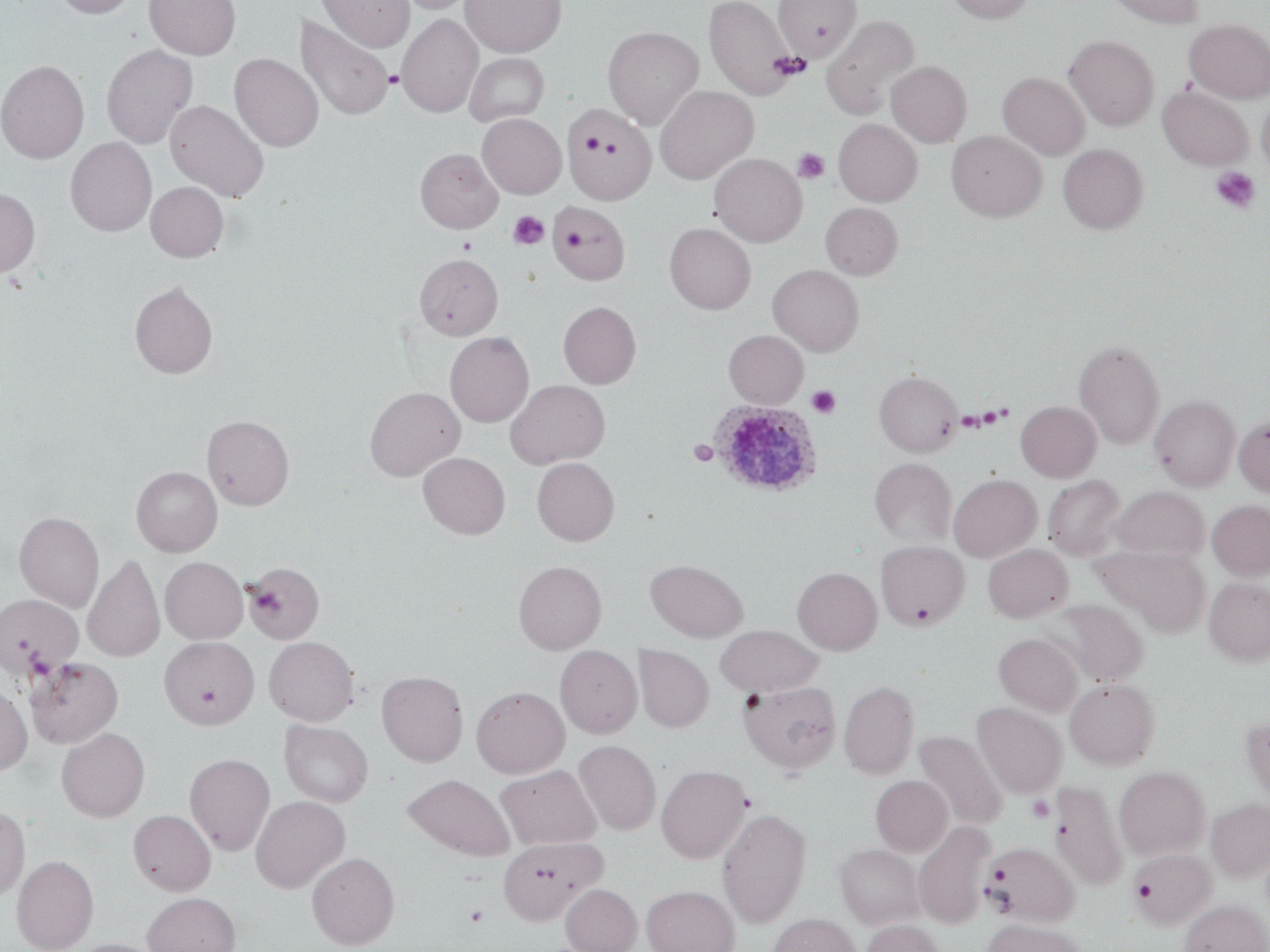

slide-level diagnosis = Plasmodium ovale
uninfected red blood cell locations = approximate bounding boxes as [x1, y1, x2, y2] in pixels: [50, 0, 138, 18], [145, 0, 241, 60], [318, 0, 415, 52], [396, 0, 477, 14], [460, 0, 566, 57], [704, 0, 796, 100], [945, 0, 1035, 24], [1104, 0, 1204, 28], [773, 1, 862, 63], [397, 14, 483, 117], [295, 15, 394, 120], [821, 15, 920, 121], [1184, 18, 1270, 103], [602, 26, 703, 129], [1064, 35, 1158, 130], [101, 44, 198, 149], [464, 52, 549, 126], [229, 53, 323, 152], [0, 59, 89, 164], [886, 61, 972, 147], [998, 71, 1090, 160], [655, 85, 759, 184], [1157, 85, 1253, 170], [1257, 93, 1270, 178], [165, 99, 270, 202], [563, 107, 656, 204], [477, 113, 566, 199], [834, 119, 922, 206], [946, 130, 1047, 222], [65, 136, 157, 236], [1058, 143, 1148, 234], [415, 148, 502, 233], [709, 153, 807, 247], [146, 181, 229, 262], [0, 188, 40, 277], [546, 200, 630, 285], [821, 202, 903, 280], [664, 223, 756, 314], [415, 253, 503, 339], [767, 264, 864, 356], [129, 281, 218, 379], [558, 301, 641, 388], [724, 330, 808, 408], [445, 331, 534, 427], [1074, 339, 1165, 449], [875, 371, 963, 457], [505, 379, 610, 469], [364, 386, 466, 481], [1150, 395, 1241, 491], [1015, 400, 1102, 482], [202, 414, 294, 510], [1234, 415, 1270, 497], [418, 452, 510, 539], [532, 457, 619, 545], [869, 458, 957, 546], [131, 466, 223, 557], [949, 474, 1042, 562], [1043, 475, 1126, 560], [1112, 486, 1209, 561], [1207, 499, 1270, 580], [14, 511, 104, 612], [875, 540, 970, 629], [982, 544, 1073, 622], [1096, 545, 1212, 637], [83, 555, 165, 663], [160, 557, 248, 644], [646, 559, 748, 643], [513, 560, 606, 654], [245, 562, 323, 644], [792, 567, 882, 655], [1204, 577, 1270, 666], [1, 594, 83, 679], [1054, 600, 1148, 686], [716, 625, 822, 697], [993, 632, 1083, 716], [264, 636, 359, 726], [160, 637, 258, 730], [555, 645, 642, 739], [633, 645, 714, 733], [25, 656, 123, 749], [376, 670, 468, 767], [1065, 678, 1160, 770], [738, 680, 842, 774], [840, 680, 919, 779], [0, 685, 33, 775], [471, 686, 569, 778], [972, 702, 1067, 798], [1240, 717, 1270, 805], [279, 720, 373, 807], [56, 728, 150, 822], [914, 731, 1008, 831], [574, 740, 661, 835], [184, 753, 275, 856], [655, 764, 751, 863], [496, 765, 601, 850], [1114, 766, 1211, 860], [403, 774, 515, 861], [870, 775, 953, 856], [1049, 780, 1128, 891], [250, 796, 350, 892], [1206, 798, 1270, 883], [0, 805, 30, 903], [716, 807, 812, 927], [128, 809, 216, 896], [913, 822, 994, 928], [498, 837, 607, 925], [987, 842, 1079, 926], [835, 843, 924, 929], [1128, 849, 1215, 930], [307, 852, 400, 950], [12, 854, 98, 952], [560, 884, 642, 952], [642, 885, 739, 952], [142, 892, 241, 952], [1179, 899, 1270, 952], [768, 913, 862, 952], [860, 919, 946, 952], [982, 919, 1088, 952], [67, 939, 166, 952]
preparation = thin blood film
platelet locations = approximate bounding boxes as [x1, y1, x2, y2] in pixels: [769, 52, 809, 79], [384, 70, 403, 89], [581, 134, 604, 154], [793, 148, 829, 184], [1211, 166, 1260, 213], [508, 211, 549, 250], [457, 237, 476, 255], [807, 385, 841, 418], [688, 440, 718, 467], [908, 601, 936, 627], [1026, 795, 1056, 823], [986, 866, 1010, 886], [465, 904, 489, 927]
magnification = 1000x
image size = 1270×952 pixels
stain = May-Grünwald-Giemsa
field of view = one of a larger specimen
Plasmodium ovale-infected red blood cell locations = approximate bounding boxes as [x1, y1, x2, y2] in pixels: [705, 405, 816, 500]
modality = optical microscopy